Comment on the morphology of the erythrocytes.
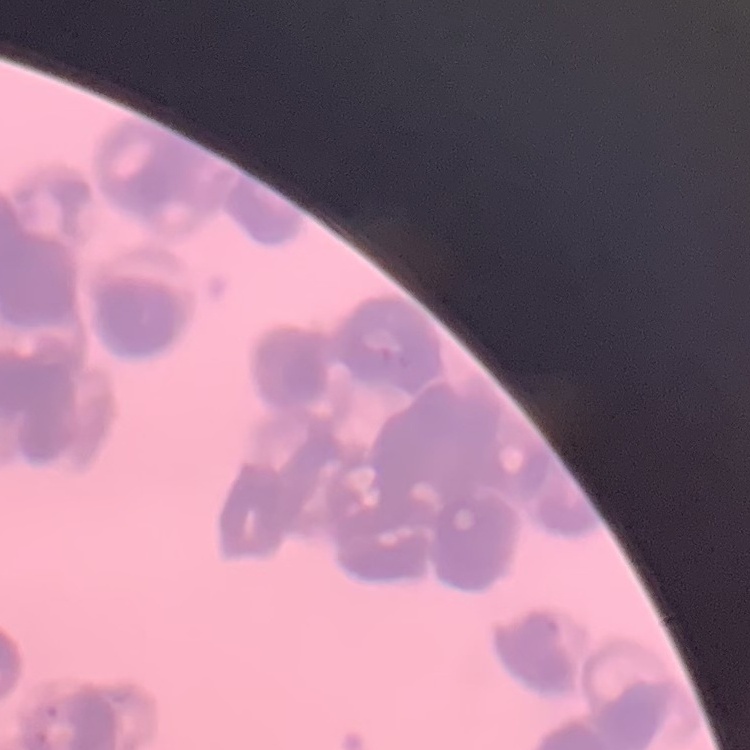
They show rouleaux formation.

Summary:
  - Stain: Field's or Giemsa
  - Preparation: thin blood smear
  - Image type: square crop of a larger photomicrograph